Locate every blood parasite and identify its species.
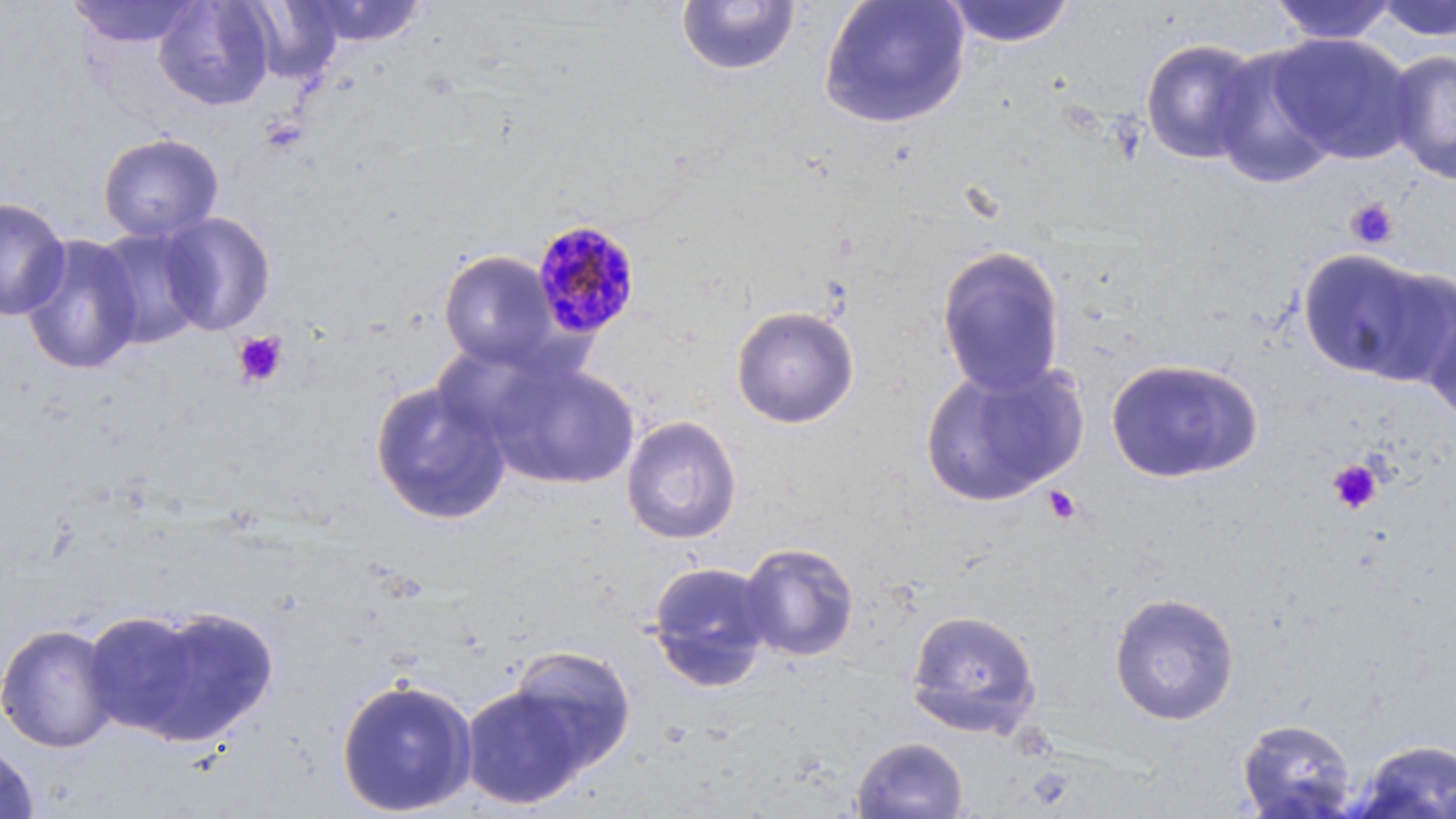

Approximate bounding boxes as (x1, y1, x2, y2) in pixels.
Plasmodium malariae-infected red blood cells: (530, 218, 642, 340).
No Plasmodium falciparum, Plasmodium ovale, Plasmodium vivax, Babesia divergens, or Trypanosoma brucei observed.

Summary:
  - Uninfected red blood cell locations: (152, 0, 275, 111), (299, 0, 427, 47), (818, 0, 971, 129), (1371, 0, 1456, 42), (68, 1, 201, 48), (240, 1, 342, 84), (675, 1, 801, 77), (941, 1, 1077, 48), (1267, 1, 1401, 45), (1269, 33, 1417, 163), (1139, 38, 1265, 165), (1207, 45, 1339, 190), (1384, 49, 1456, 185), (98, 132, 224, 243), (0, 196, 71, 321), (158, 211, 277, 336), (91, 225, 210, 350), (19, 233, 144, 376), (936, 245, 1066, 397), (1296, 247, 1453, 386), (438, 250, 561, 369), (1420, 297, 1456, 427), (730, 305, 860, 428), (482, 357, 641, 491), (1105, 357, 1263, 484), (918, 359, 1089, 508), (369, 379, 512, 526), (621, 415, 742, 545), (738, 542, 860, 662), (646, 560, 774, 692), (1109, 591, 1239, 726), (112, 603, 280, 748), (905, 608, 1041, 738), (0, 621, 119, 754), (504, 645, 638, 774), (335, 676, 478, 817), (460, 683, 592, 810), (1236, 717, 1358, 818), (851, 736, 969, 819), (1350, 738, 1456, 818), (0, 744, 39, 818)
  - Platelet locations: (1345, 197, 1400, 250), (232, 330, 288, 388), (1327, 459, 1383, 514), (1043, 485, 1083, 526)
  - Slide-level diagnosis: Plasmodium malariae
  - Modality: light microscopy
  - Stain: May-Grünwald-Giemsa
  - Preparation: thin blood smear
  - Magnification: 1000x
  - Image size: 1456×819 pixels
  - Field of view: one of a larger specimen